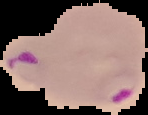

Summary:
  - Image size: 148×115 pixels
  - Image type: segmented cell region on a black background
  - Malaria status: parasitized
  - Preparation: thin blood film